Name the parasite shown.
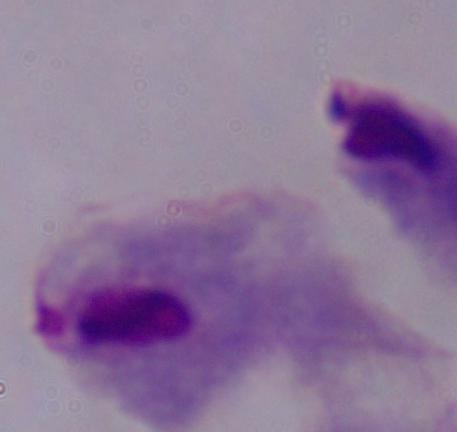
A trichomonad.

Summary:
  - Magnification: 1000x
  - Modality: micrograph